Give the extent of all Plasmodium vivax-infected red blood cells.
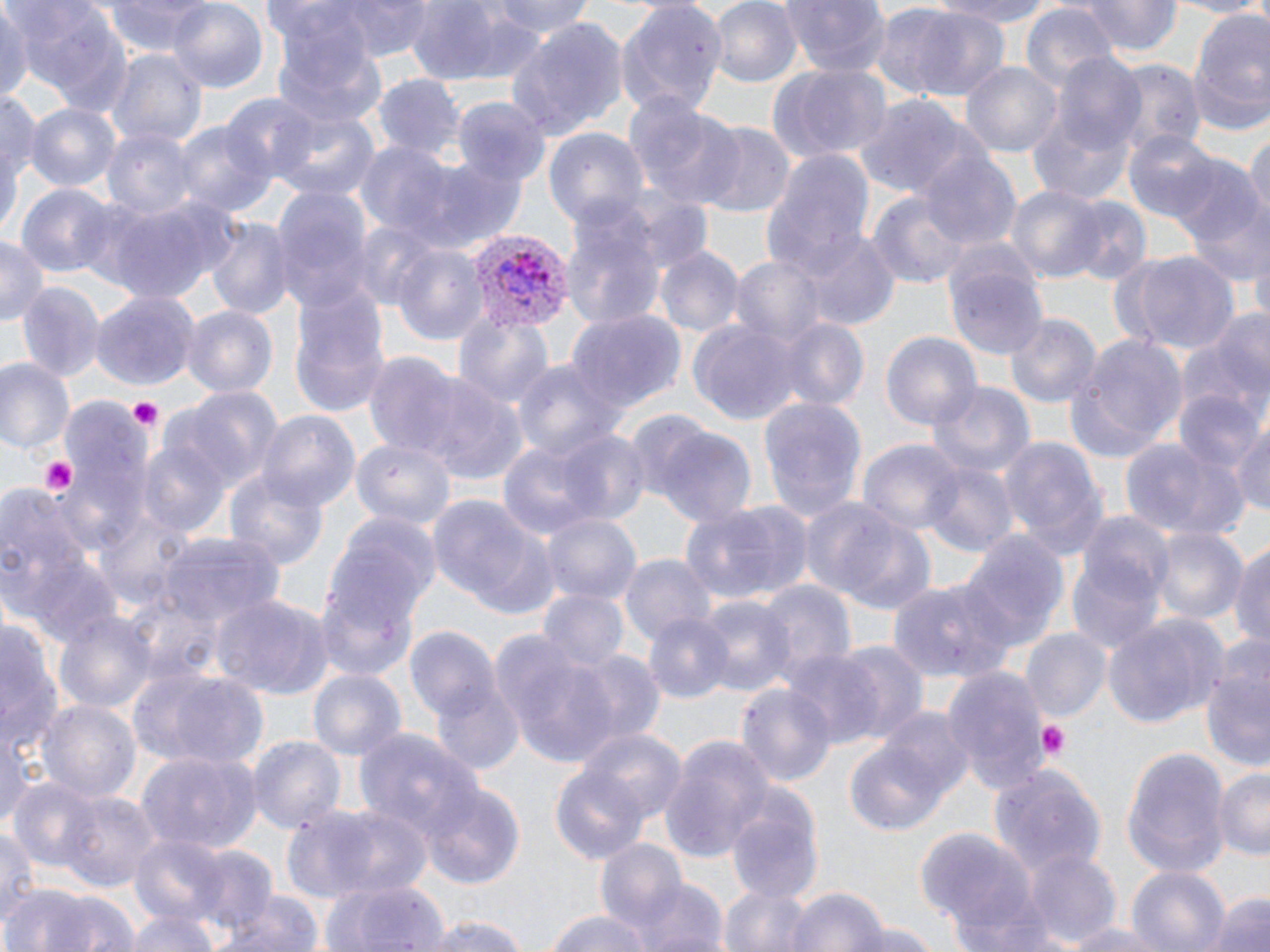
Approximate bounding boxes as (x1, y1, x2, y2) in pixels.
Plasmodium vivax-infected red blood cells: (463, 225, 574, 333).

slide-level diagnosis = Plasmodium vivax
field of view = one of a larger specimen
uninfected red blood cell locations = approximate bounding boxes as (x1, y1, x2, y2) in pixels: (0, 0, 31, 108), (9, 0, 132, 113), (103, 0, 220, 58), (313, 0, 440, 60), (488, 0, 594, 38), (708, 0, 802, 89), (782, 0, 890, 78), (928, 0, 1063, 27), (1082, 0, 1180, 56), (1164, 0, 1269, 16), (402, 1, 540, 86), (167, 2, 271, 93), (618, 2, 727, 119), (1021, 3, 1119, 96), (905, 8, 1013, 104), (1184, 10, 1270, 136), (266, 12, 387, 130), (503, 17, 628, 138), (106, 49, 206, 152), (1053, 56, 1151, 156), (1108, 61, 1204, 157), (961, 62, 1064, 159), (770, 63, 891, 164), (375, 76, 464, 163), (2, 88, 38, 212), (222, 90, 316, 181), (855, 95, 970, 200), (629, 97, 750, 211), (454, 98, 547, 184), (25, 103, 119, 194), (271, 107, 381, 206), (1026, 107, 1133, 205), (177, 122, 276, 218), (693, 122, 796, 218), (103, 126, 198, 219), (1122, 126, 1220, 223), (1245, 126, 1269, 235), (543, 128, 649, 232), (355, 142, 455, 236), (762, 150, 878, 280), (921, 151, 1022, 251), (1169, 153, 1265, 281), (414, 158, 529, 253), (1006, 183, 1108, 285), (19, 184, 117, 279), (273, 185, 375, 311), (868, 193, 972, 288), (98, 197, 234, 305), (1063, 197, 1150, 287), (559, 198, 665, 328), (203, 217, 293, 321), (793, 229, 902, 333), (0, 236, 45, 327), (391, 244, 488, 348), (657, 246, 743, 337), (1128, 251, 1239, 354), (729, 256, 826, 350), (946, 259, 1049, 364), (15, 280, 104, 382), (289, 288, 391, 420), (90, 291, 196, 389), (182, 306, 277, 400), (566, 308, 683, 415), (454, 309, 557, 414), (769, 313, 868, 413), (1005, 314, 1099, 408), (1182, 316, 1268, 438), (689, 320, 800, 426), (1068, 328, 1190, 459), (882, 330, 982, 432), (362, 354, 472, 461), (0, 355, 76, 454), (510, 358, 620, 464), (416, 372, 528, 482), (922, 380, 1036, 483), (175, 386, 285, 493), (1172, 390, 1265, 482), (55, 397, 150, 548), (759, 397, 867, 523), (258, 412, 358, 511), (642, 416, 757, 526), (1231, 419, 1270, 523), (494, 429, 635, 543), (1000, 434, 1107, 562), (1119, 436, 1244, 541), (350, 438, 456, 529), (135, 440, 230, 538), (859, 440, 964, 541), (919, 462, 1015, 553), (225, 470, 332, 575), (0, 486, 101, 637), (430, 494, 556, 622), (681, 499, 812, 606), (821, 509, 942, 618), (322, 511, 440, 639), (540, 513, 641, 608), (1068, 523, 1171, 654), (955, 526, 1067, 660), (1150, 526, 1247, 625), (157, 532, 282, 636), (1185, 535, 1269, 638), (1231, 542, 1270, 658), (621, 553, 716, 646), (316, 565, 425, 681), (885, 579, 1016, 680), (757, 581, 854, 685), (536, 588, 627, 673), (212, 595, 333, 698), (696, 596, 794, 695), (54, 610, 157, 716), (642, 611, 735, 705), (1104, 612, 1230, 729), (0, 616, 60, 766), (407, 623, 500, 721), (1022, 629, 1112, 723), (491, 636, 619, 766), (1197, 640, 1270, 777), (831, 643, 928, 744), (566, 649, 666, 751), (783, 650, 886, 745), (127, 663, 267, 772), (307, 667, 406, 762), (943, 667, 1050, 796), (431, 677, 525, 773), (737, 681, 837, 787), (36, 697, 141, 805), (845, 722, 964, 840), (576, 726, 688, 823), (353, 727, 484, 842), (0, 731, 33, 827), (249, 736, 345, 837), (660, 737, 775, 859), (1119, 746, 1232, 879), (136, 752, 260, 857), (990, 760, 1112, 882), (548, 764, 649, 866), (1212, 765, 1270, 862), (8, 778, 102, 869), (418, 781, 528, 892), (724, 786, 823, 899), (56, 791, 160, 891), (322, 805, 436, 900), (279, 806, 383, 902), (1, 823, 40, 931), (914, 826, 1034, 937), (129, 834, 231, 931), (595, 839, 691, 936), (187, 846, 276, 938), (1025, 848, 1120, 948), (1124, 868, 1229, 952), (625, 875, 728, 952), (321, 876, 450, 952), (8, 882, 138, 952), (721, 884, 815, 952), (786, 886, 890, 952), (214, 889, 328, 952), (1202, 889, 1270, 952), (952, 893, 1069, 952), (123, 904, 221, 952), (543, 908, 655, 952), (421, 913, 535, 952), (838, 918, 945, 951), (1061, 920, 1180, 951)
magnification = 1000x
image size = 1270×952 pixels
platelet locations = approximate bounding boxes as (x1, y1, x2, y2) in pixels: (125, 397, 163, 434), (39, 456, 81, 498), (1038, 720, 1071, 758)
preparation = thin blood smear
stain = May-Grünwald-Giemsa
modality = optical microscopy